Name the blood parasite species.
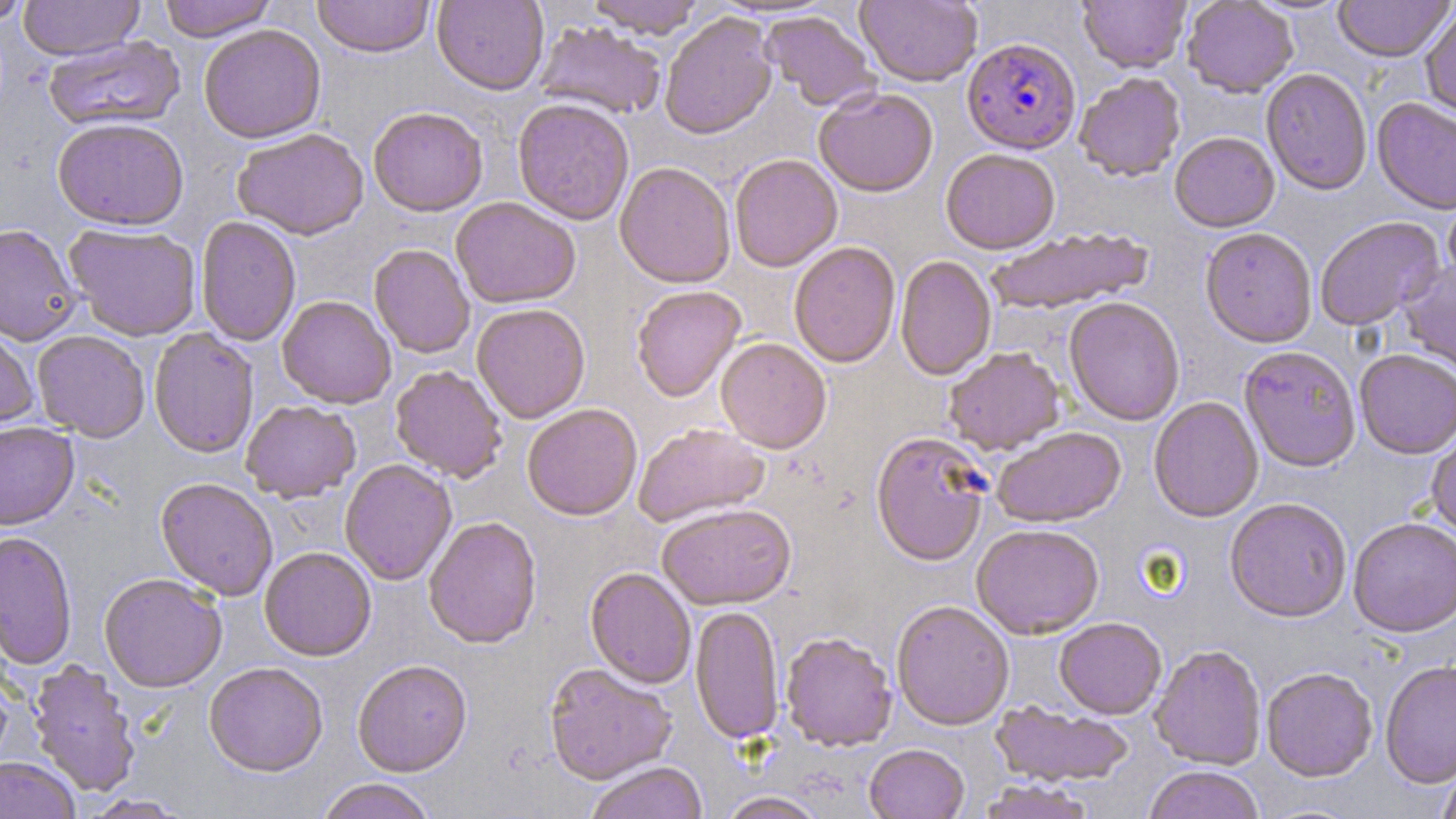

Plasmodium falciparum.

{
  "image_size": "1456×819 pixels",
  "field_of_view": "single",
  "preparation": "thin blood film",
  "stain": "May-Grünwald-Giemsa",
  "uninfected_red_blood_cell_locations": "approximate bounding boxes as (x1,y1)-(x2,y2) corner pairs in pixels: (0,0)-(32,27), (19,0)-(144,61), (158,0)-(277,42), (312,0)-(435,59), (432,0)-(549,95), (585,0)-(706,39), (855,0)-(982,88), (1078,0)-(1191,74), (1183,0)-(1298,98), (1333,0)-(1454,63), (1421,7)-(1456,123), (659,12)-(777,141), (760,12)-(878,112), (534,21)-(667,119), (199,24)-(326,144), (43,35)-(185,133), (1261,67)-(1373,196), (1074,73)-(1186,183), (814,88)-(938,198), (1372,98)-(1456,216), (512,99)-(634,226), (368,107)-(488,217), (52,118)-(189,232), (232,129)-(369,241), (1169,132)-(1280,233), (940,150)-(1060,255), (729,155)-(842,273), (615,162)-(735,289), (1443,195)-(1456,288), (450,197)-(581,309), (1315,216)-(1444,331), (195,217)-(301,347), (0,224)-(81,346), (64,224)-(201,341), (1200,227)-(1317,349), (987,228)-(1152,315), (789,242)-(901,369), (369,244)-(475,359), (895,256)-(997,380), (1399,258)-(1456,379), (631,286)-(745,403), (277,296)-(396,409), (1064,298)-(1185,426), (472,304)-(590,424), (0,326)-(39,433), (148,328)-(259,458), (32,331)-(150,442), (716,338)-(832,453), (1238,346)-(1362,472), (943,348)-(1066,456), (1354,349)-(1456,459), (390,366)-(507,483), (1149,396)-(1263,524), (241,400)-(361,503), (522,405)-(642,521), (0,421)-(79,530), (633,424)-(769,527), (991,427)-(1126,529), (1426,430)-(1456,541), (870,432)-(991,567), (339,460)-(457,586), (155,478)-(278,601), (1224,498)-(1352,623), (657,504)-(796,611), (424,517)-(542,649), (1348,519)-(1456,639), (971,525)-(1104,641), (0,531)-(77,670), (259,548)-(376,662), (585,568)-(696,689), (99,574)-(227,692), (891,601)-(1015,731), (690,606)-(784,744), (1053,618)-(1167,720), (779,624)-(1012,738), (781,633)-(897,753), (1150,645)-(1266,769), (27,661)-(141,798), (353,661)-(472,778), (1380,661)-(1456,790), (544,663)-(677,786), (204,664)-(328,779), (1261,668)-(1378,782), (990,701)-(1134,788), (864,744)-(970,819), (0,757)-(79,819), (585,762)-(708,819), (1438,763)-(1456,819), (1144,767)-(1265,819), (317,779)-(436,819), (976,780)-(1096,819), (717,792)-(827,819), (79,794)-(191,818)",
  "modality": "optical microscopy",
  "plasmodium_falciparum_infected_red_blood_cell_locations": "approximate bounding boxes as (x1,y1)-(x2,y2) corner pairs in pixels: (961,39)-(1081,155)",
  "magnification": "1000x"
}